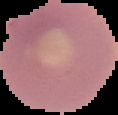 The area outside the segmented cell region is set to black. Malaria status: uninfected. From a thin blood film. Image is 118×115 pixels.